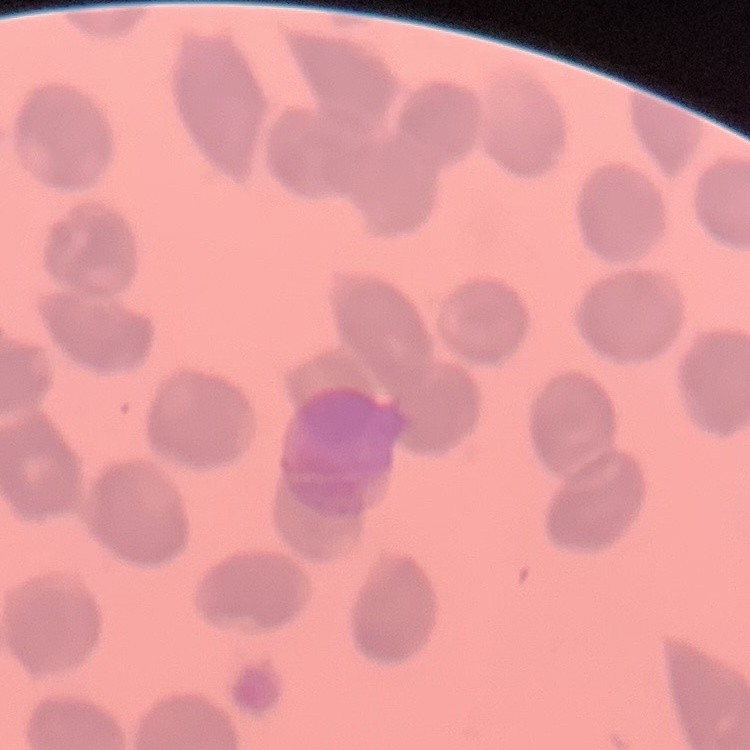

erythrocyte_morphology: no rouleaux formation
preparation: thin blood film
stain: Field's or Giemsa
image_type: one tile cut from a larger photomicrograph